Locate every Trypanosoma brucei.
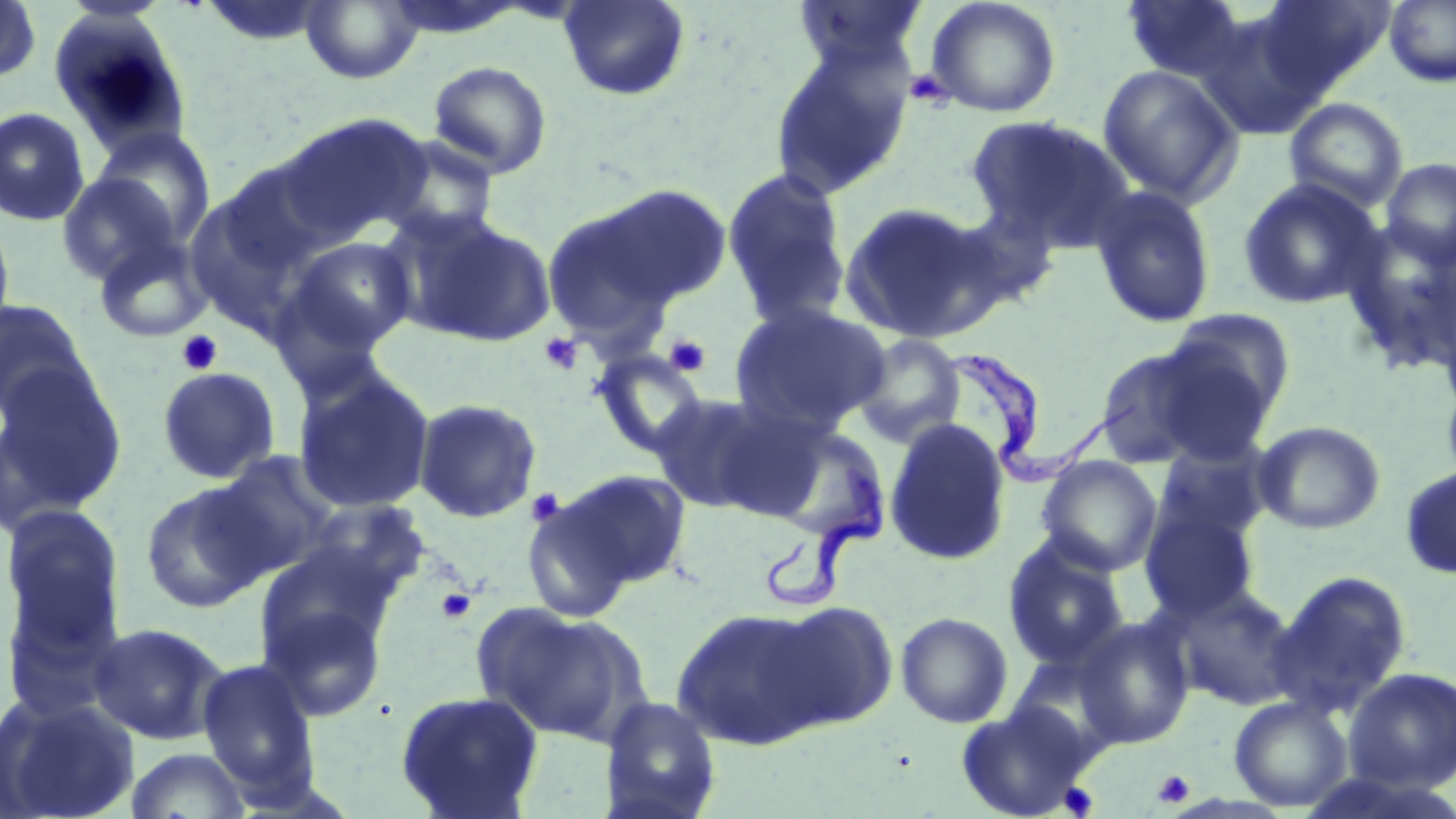
Approximate bounding boxes as [x1, y1, x2, y2] in pixels.
Trypanosoma brucei: [948, 349, 1137, 484], [763, 459, 886, 614].

Summary:
  - Platelet locations: [904, 69, 953, 108], [176, 330, 223, 375], [539, 332, 583, 375], [663, 333, 712, 378], [525, 487, 567, 527], [436, 588, 476, 624], [1153, 769, 1195, 807], [1058, 782, 1099, 817]
  - Uninfected red blood cell locations: [0, 0, 42, 85], [301, 0, 423, 84], [558, 0, 691, 102], [926, 0, 1061, 118], [1120, 0, 1251, 84], [1252, 0, 1394, 97], [1383, 0, 1456, 87], [790, 1, 932, 76], [199, 2, 329, 47], [1197, 11, 1330, 136], [49, 12, 193, 156], [768, 34, 917, 200], [428, 61, 552, 178], [1097, 64, 1244, 207], [1283, 97, 1409, 213], [0, 107, 91, 227], [273, 112, 432, 244], [966, 115, 1133, 251], [89, 127, 216, 253], [376, 136, 501, 245], [1380, 157, 1456, 267], [720, 167, 852, 329], [55, 171, 182, 286], [1237, 177, 1384, 309], [590, 183, 734, 307], [1089, 185, 1217, 328], [183, 189, 316, 337], [837, 200, 1002, 343], [540, 202, 685, 351], [944, 205, 1063, 311], [0, 208, 16, 345], [399, 214, 557, 349], [92, 232, 214, 344], [281, 235, 418, 360], [0, 298, 96, 421], [729, 302, 891, 434], [1161, 306, 1298, 430], [851, 334, 967, 448], [1092, 342, 1234, 467], [590, 347, 711, 461], [0, 365, 127, 522], [157, 366, 281, 484], [292, 366, 436, 515], [1441, 371, 1456, 494], [650, 392, 786, 514], [412, 397, 543, 524], [883, 418, 1012, 566], [763, 421, 892, 545], [1253, 421, 1386, 535], [1151, 443, 1271, 547], [211, 450, 343, 575], [1036, 455, 1163, 576], [1399, 464, 1456, 580], [557, 469, 693, 591], [139, 480, 272, 614], [520, 489, 639, 624], [297, 500, 430, 611], [1, 505, 127, 651], [1139, 508, 1260, 621], [1002, 539, 1130, 669], [1269, 570, 1412, 717], [1172, 585, 1301, 710], [259, 598, 389, 722], [768, 600, 899, 731], [479, 605, 647, 746], [671, 606, 829, 750], [895, 611, 1013, 728], [1075, 616, 1196, 749], [88, 622, 229, 745], [196, 657, 323, 802], [1343, 667, 1456, 793], [394, 690, 545, 819], [1, 691, 140, 819], [600, 695, 722, 819], [1228, 695, 1353, 812], [954, 701, 1094, 819], [124, 746, 252, 819]
  - Slide-level diagnosis: Trypanosoma brucei
  - Stain: May-Grünwald-Giemsa
  - Image size: 1456×819 pixels
  - Magnification: 1000x
  - Field of view: one of a larger specimen
  - Modality: optical microscopy
  - Preparation: thin blood film